Report the malaria status of this cell.
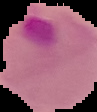
Parasitized.

Segmented cell region on a black background. Image is 97×112 pixels. From a thin blood film.